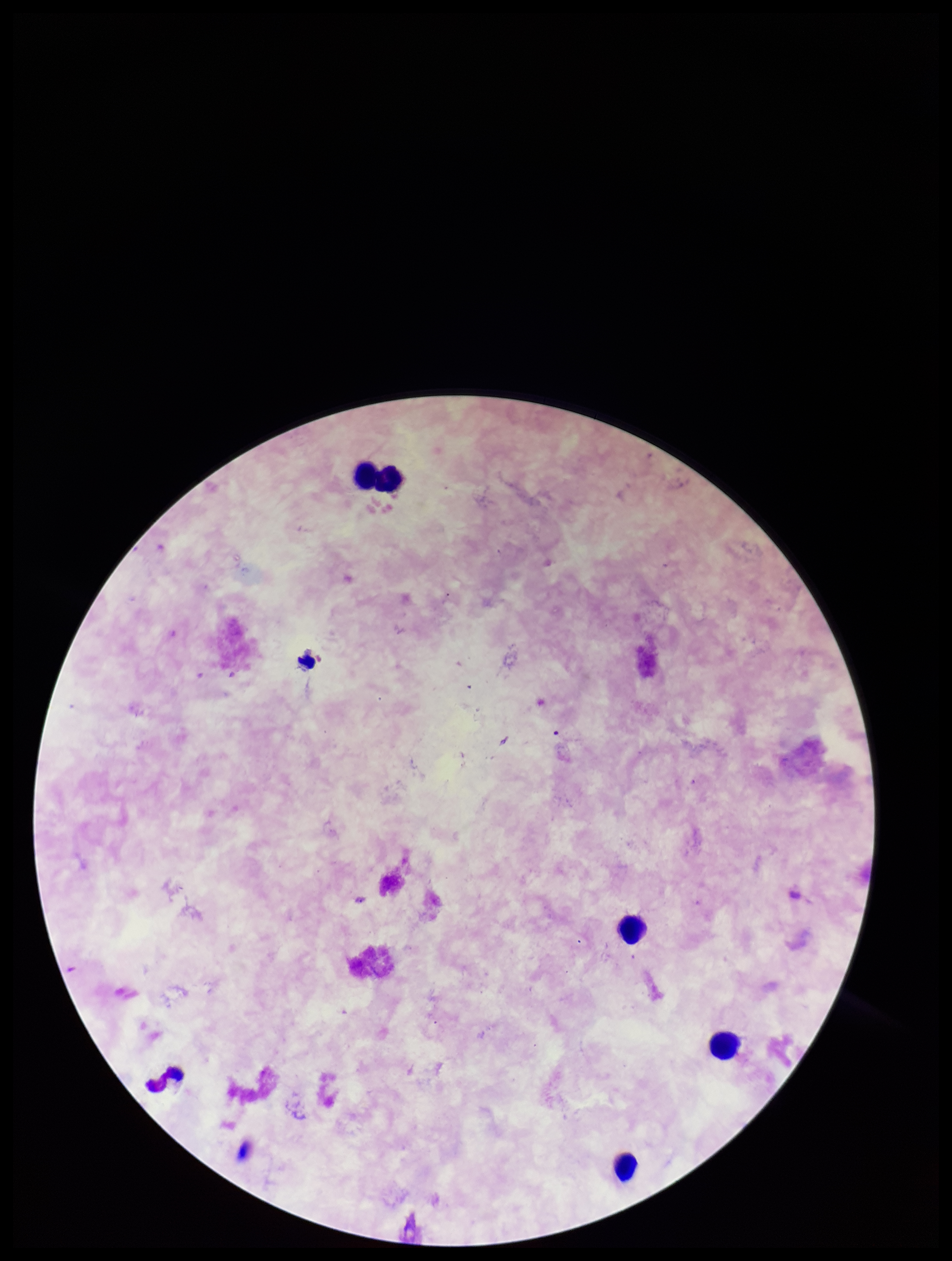
Summary:
  - Preparation: thick
  - Leukocyte count: 5
  - Patient malaria status: negative
  - Plasmodium parasites: none identified
  - Parasite count: 0
  - Field of view: one from this slide
  - Capture: smartphone photograph through the microscope eyepiece
  - Stain: Giemsa
  - Image size: 952×1261 pixels